Describe the morphology of the red blood cells.
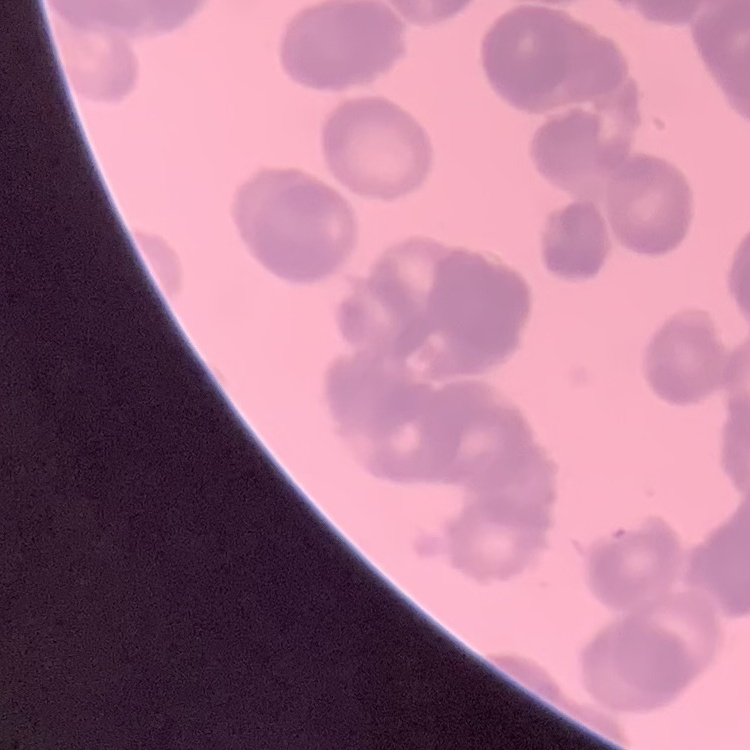

They show rouleaux formation.

stain = Field's or Giemsa
preparation = thin blood smear
image type = one tile cut from a larger photomicrograph